Identify the cell.
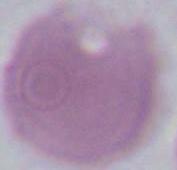
This is an erythrocyte.

Micrograph. 1000x magnification.